Describe the morphology of the red blood cells.
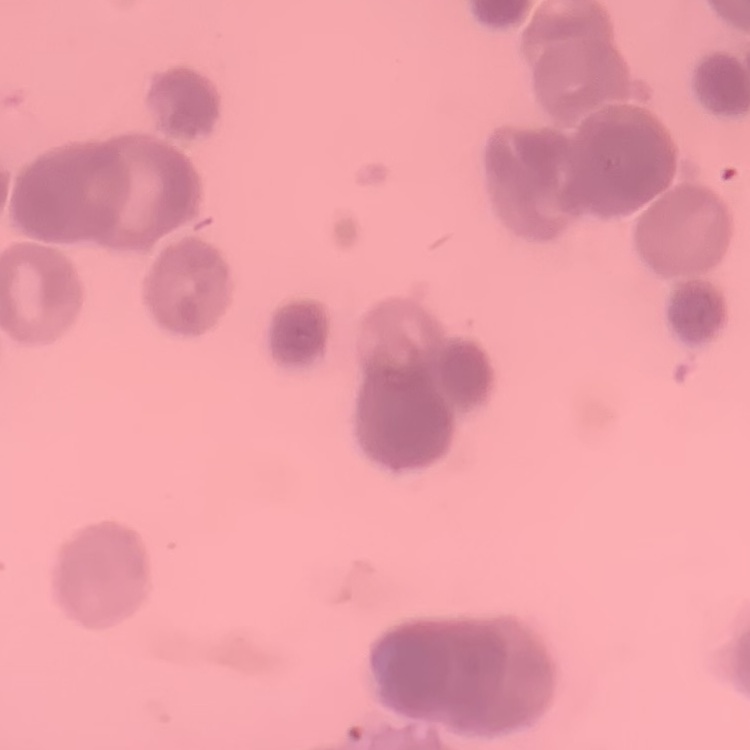
They show rouleaux formation.

image_type: square crop of a larger photomicrograph
stain: Field's or Giemsa
preparation: thin peripheral smear